Classify this cell by malaria status.
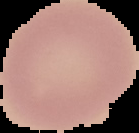
It is uninfected.

Summary:
  - Image type: cell region segmented out of the field of view; surrounding area masked to black
  - Preparation: thin blood smear
  - Image size: 139×133 pixels